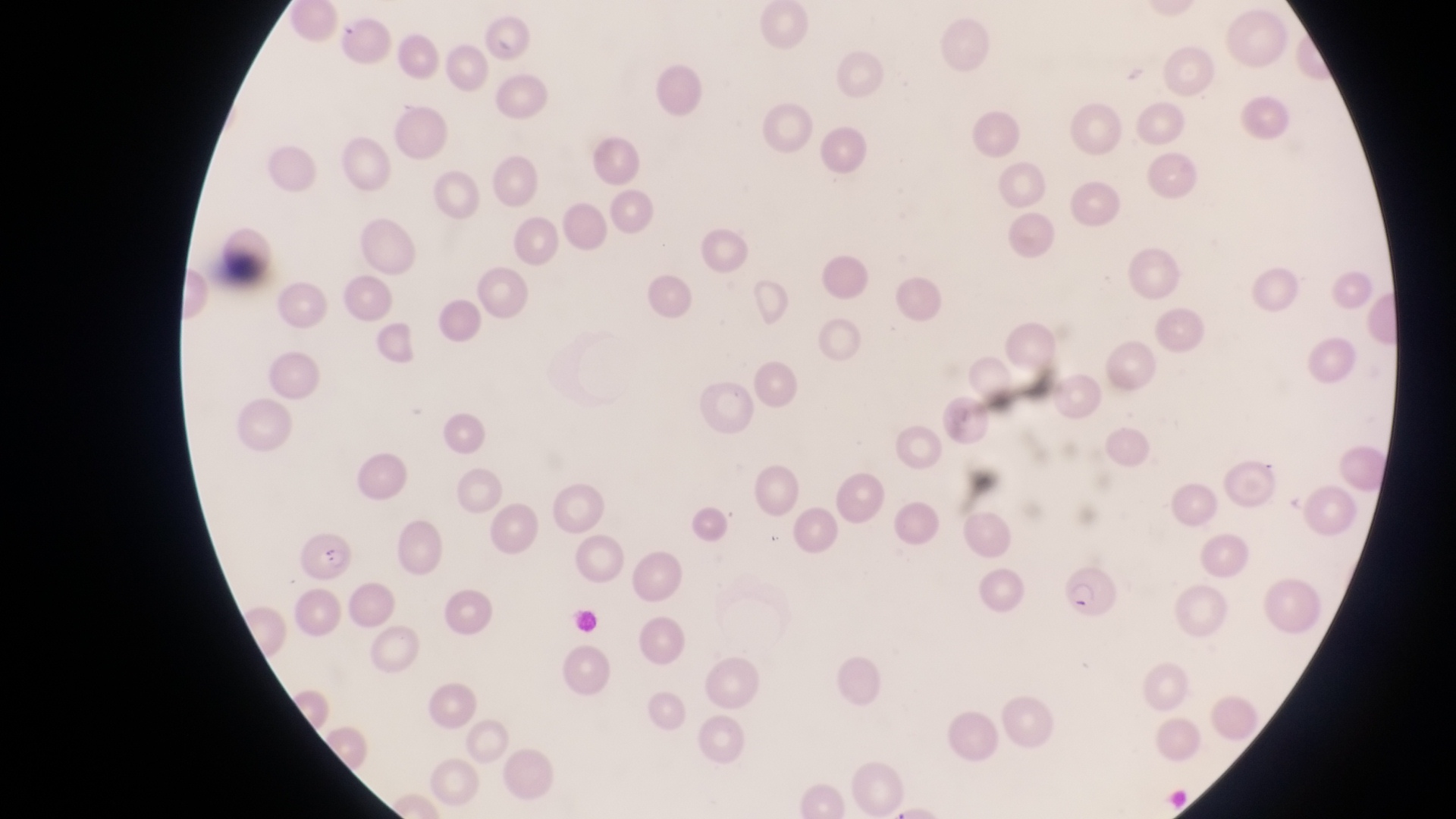
Approximate bounding boxes as left top right bottom in pixels.
Summary:
  - Parasitised red blood cell locations: 297 529 358 585; 1065 563 1123 630
  - Trophozoite locations: 338 16 362 37
  - Preparation: thin blood smear
  - Field of view: single
  - Image size: 1456×819 pixels
  - Country: Uganda
  - Magnification: 1000x
  - Capture: smartphone photograph through the eyepiece of an Olympus CX-23 microscope